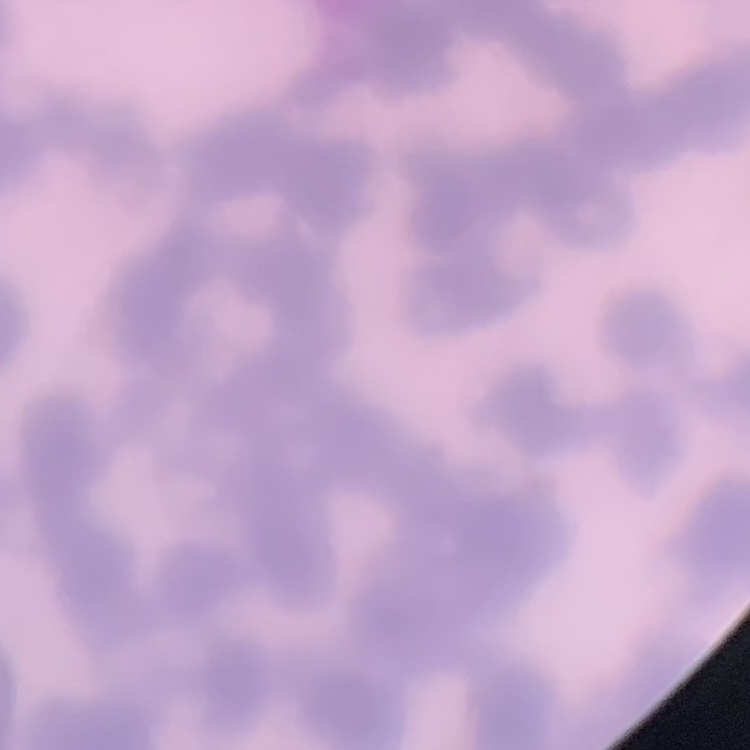

red blood cell morphology = rouleaux formation
stain = Field's or Giemsa
image type = one tile cut from a larger photomicrograph
preparation = thin blood film